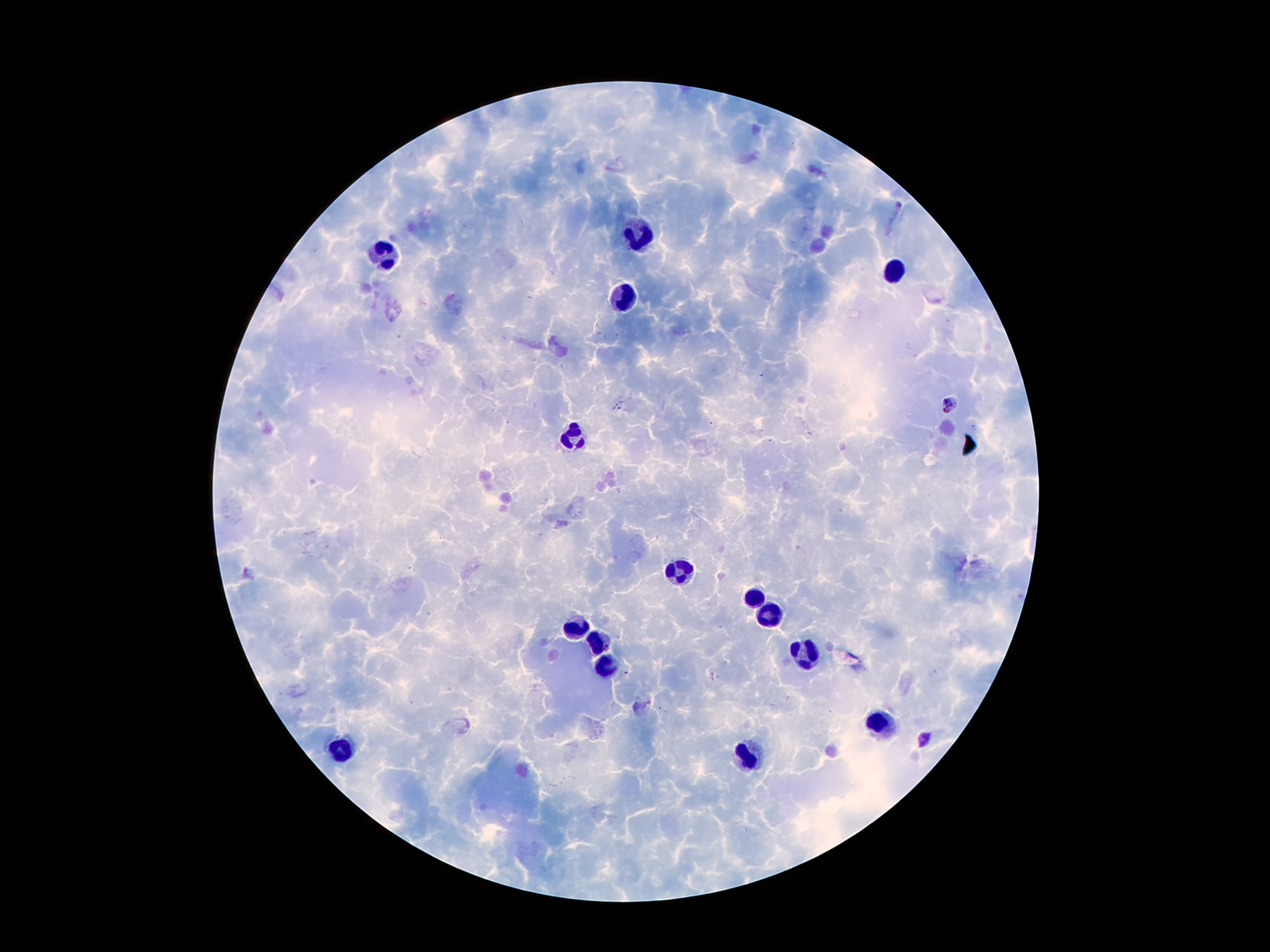

Approximate centers as (x, y) in pixels.
Summary:
  - Leukocyte locations: (641, 231), (389, 255), (898, 268), (621, 302), (572, 433), (676, 569), (752, 596), (769, 616), (577, 628), (599, 641), (804, 650), (606, 668), (878, 725), (344, 747), (745, 759)
  - Plasmodium parasite locations: (948, 403), (625, 672), (926, 740)
  - Stain: Giemsa
  - Image size: 1270×952 pixels
  - Capture: smartphone through the microscope eyepiece
  - Field of view: one from this slide
  - Patient malaria status: infected with Plasmodium falciparum
  - Preparation: thick blood smear
  - Magnification: 100x